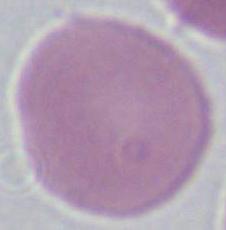

Photomicrograph. Captured at 1000x magnification. A red blood cell is seen.